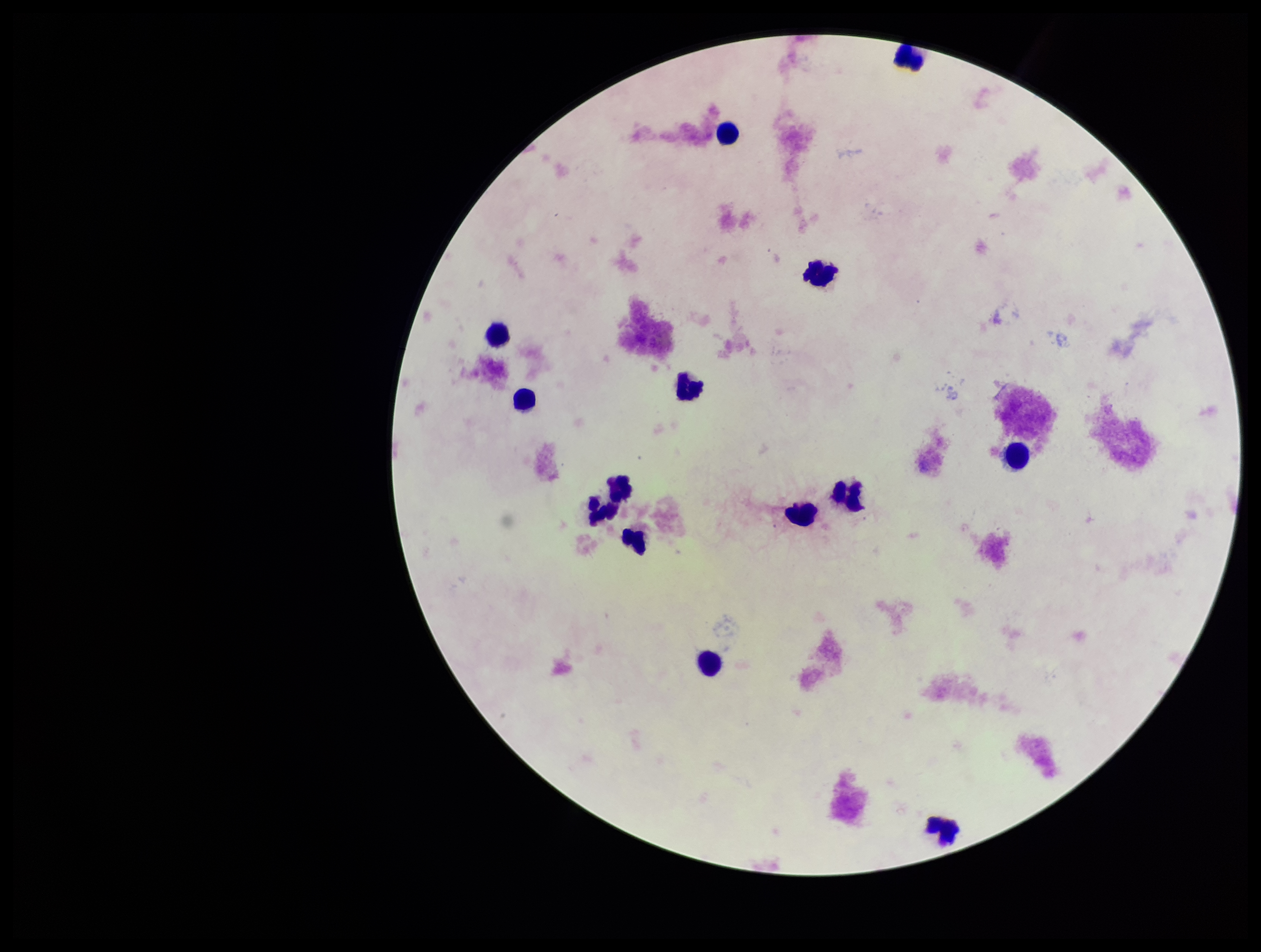
Plasmodium parasites: none seen. Parasite count: 0. Photographed through the microscope eyepiece with a smartphone camera. Stained with Giemsa. Leukocyte count: 14. Preparation: thick blood smear. Patient malaria status: negative. Image is 1261×952 pixels. One field from this slide.